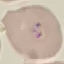

Malaria status: parasitized. Giemsa-stained preparation. Acquired by smartphone through the microscope eyepiece. Thin blood smear. Cell patch, automatically extracted from a larger field of view and resized to 64 × 64 pixels.